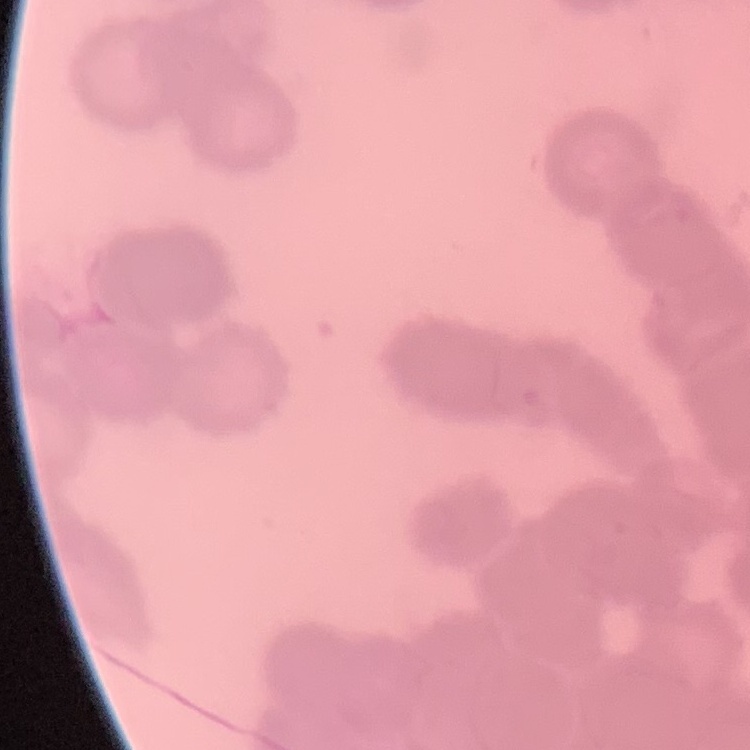
The erythrocytes show rouleaux formation. Field's or Giemsa stain. One tile cut from a larger photomicrograph. Thin blood film.